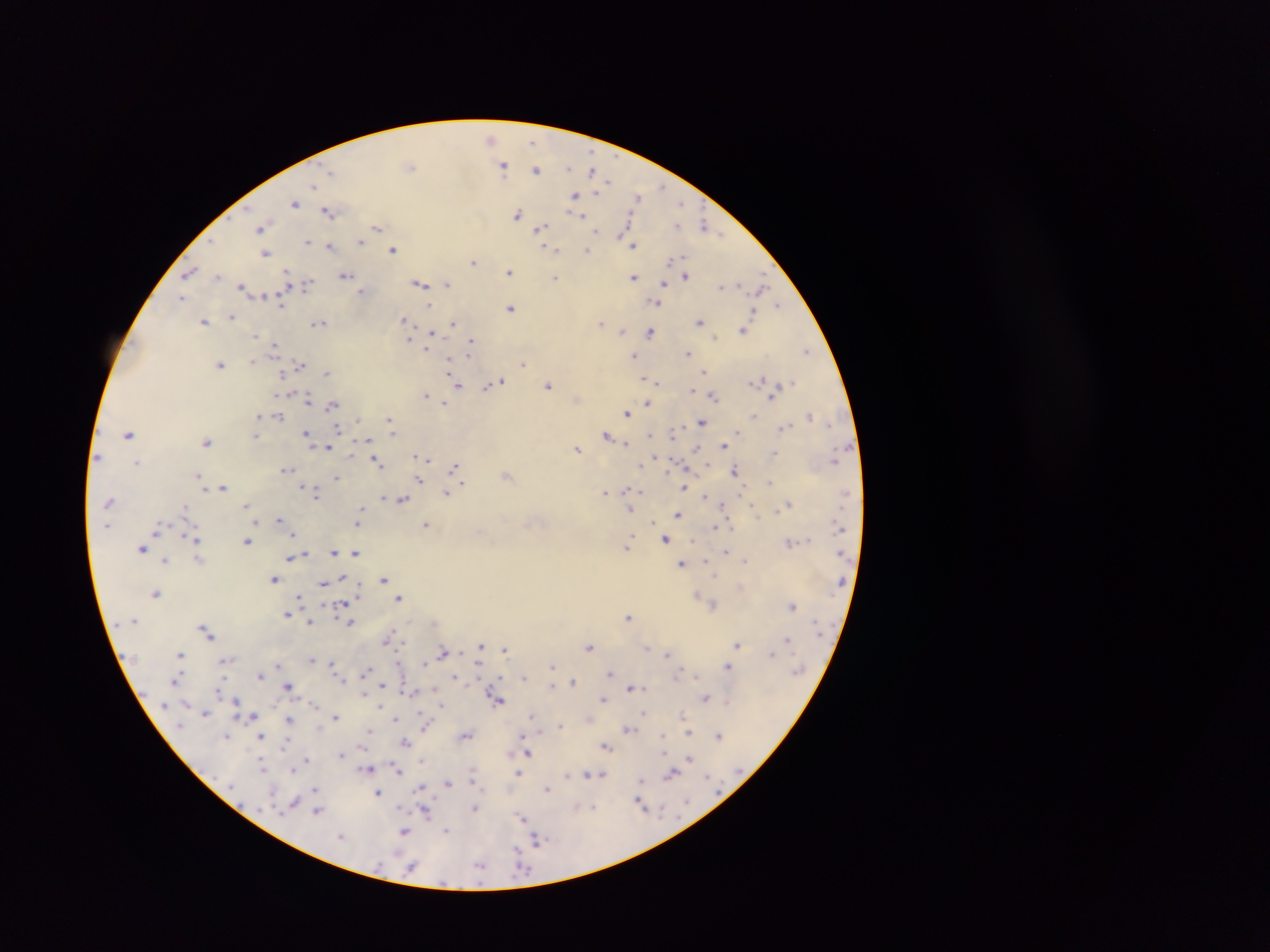

Approximate centers as x y in pixels. Plasmodium parasite locations: 491 139; 533 140; 503 165; 410 166; 568 168; 536 169; 593 172; 312 185; 661 187; 598 189; 575 194; 638 197; 295 203; 679 203; 329 212; 519 214; 579 215; 706 224; 627 225; 262 227; 376 227; 540 227; 597 231; 630 238; 307 241; 360 241; 633 244; 330 247; 554 248; 393 249; 587 250; 266 252; 672 259; 474 261; 188 271; 510 272; 346 274; 686 275; 217 276; 634 276; 555 278; 289 279; 447 283; 664 283; 306 284; 421 284; 723 286; 242 287; 761 287; 287 289; 362 290; 182 298; 282 301; 657 301; 779 304; 511 307; 756 311; 231 316; 404 319; 700 321; 204 322; 318 322; 454 323; 601 323; 743 329; 622 331; 432 332; 650 332; 409 339; 472 340; 274 347; 427 347; 806 351; 688 352; 635 354; 449 360; 253 362; 523 362; 221 364; 300 364; 705 371; 327 372; 283 374; 645 377; 762 380; 502 381; 656 382; 496 383; 457 384; 487 385; 548 385; 694 391; 425 394; 714 395; 772 395; 308 400; 576 400; 444 401; 648 402; 333 404; 628 412; 258 415; 809 415; 279 416; 755 417; 701 421; 389 423; 338 428; 785 428; 307 432; 393 432; 128 433; 651 433; 739 433; 607 434; 672 434; 256 436; 369 440; 207 441; 625 442; 724 446; 695 447; 329 448; 577 448; 417 456; 655 456; 425 459; 376 460; 138 462; 641 464; 454 467; 285 469; 736 470; 199 474; 507 474; 336 477; 419 479; 770 481; 464 483; 203 487; 223 487; 684 488; 629 490; 313 491; 448 493; 605 493; 704 495; 384 496; 402 499; 247 504; 789 504; 724 505; 361 509; 630 511; 678 514; 359 516; 279 519; 256 521; 359 521; 427 524; 716 527; 157 531; 294 535; 195 539; 665 539; 247 541; 789 542; 628 547; 142 548; 334 551; 726 551; 355 552; 306 553; 289 557; 198 559; 165 560; 745 560; 683 563; 343 577; 275 578; 383 580; 323 581; 156 594; 698 595; 399 597; 300 598; 345 604; 791 606; 287 614; 628 616; 310 623; 351 623; 206 632; 390 636; 788 639; 737 645; 481 646; 590 646; 647 646; 504 648; 444 652; 668 653; 773 653; 180 655; 312 660; 225 661; 331 662; 425 662; 481 662; 277 665; 727 665; 552 666; 366 672; 610 673; 260 675; 696 676; 525 677; 455 679; 176 680; 573 682; 288 685; 382 685; 551 686; 434 687; 632 688; 405 691; 219 693; 363 694; 706 697; 497 698; 604 699; 237 700; 729 700; 314 704; 441 704; 204 712; 644 712; 250 716; 289 717; 336 717; 590 717; 395 719; 426 725; 560 725; 628 729; 370 730; 689 733; 466 734; 522 734; 663 734; 226 735; 719 735; 261 736; 406 742; 285 746; 607 746; 529 753; 511 754; 341 755; 423 758; 689 758; 307 760; 263 766; 291 768; 369 768; 397 770; 519 773; 672 773; 567 774; 601 774; 473 777; 642 781; 448 782; 315 788; 421 788; 547 790; 378 792; 294 802; 641 803; 576 806; 474 808; 317 811; 426 811; 523 819; 448 830; 405 831; 538 840; 519 851; 481 865. Sample from Ghana. One field of view. Thick blood film. Photographed through a microscope with a mobile-phone camera. Image is 1270×952 pixels.